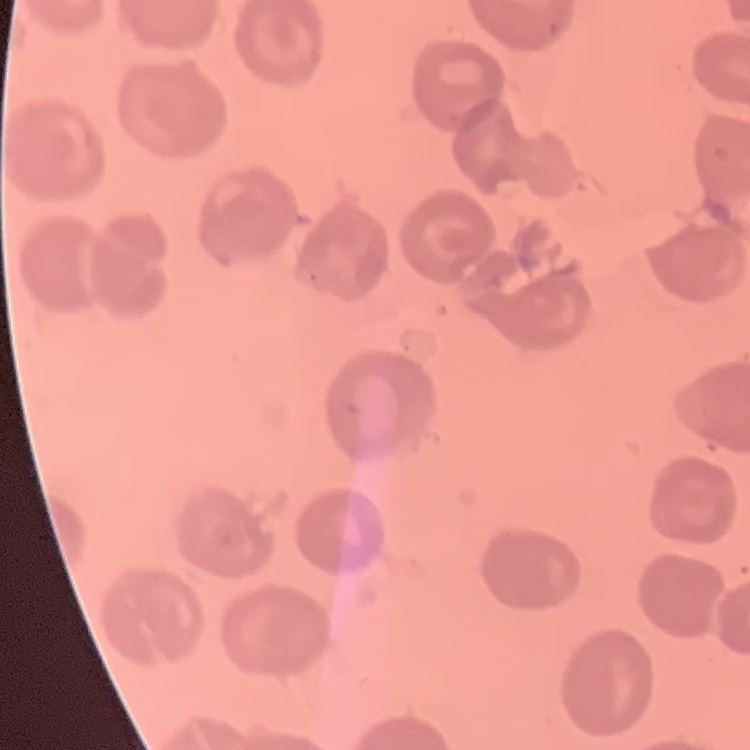

Summary:
  - Erythrocyte morphology: no rouleaux formation
  - Preparation: thin blood film
  - Stain: Field's or Giemsa
  - Image type: one tile cut from a larger photomicrograph